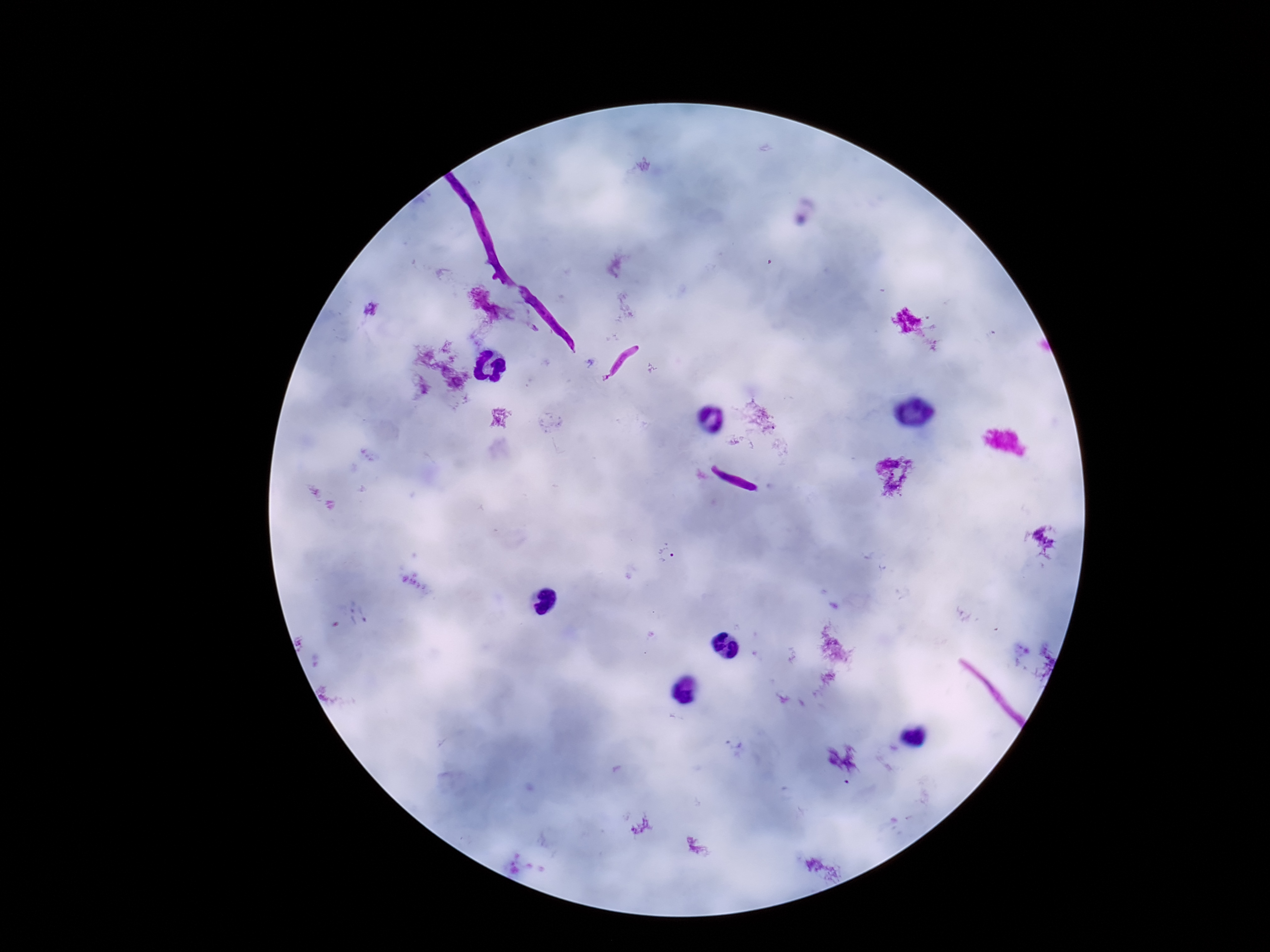
Approximate centers as {x, y} in pixels.
Summary:
  - Plasmodium parasite locations: {670, 557}
  - Field of view: single
  - Image size: 1270×952 pixels
  - Patient malaria status: positive
  - Stain: Giemsa
  - Capture: smartphone camera through the microscope eyepiece
  - Magnification: 100x
  - Preparation: thick peripheral-blood smear